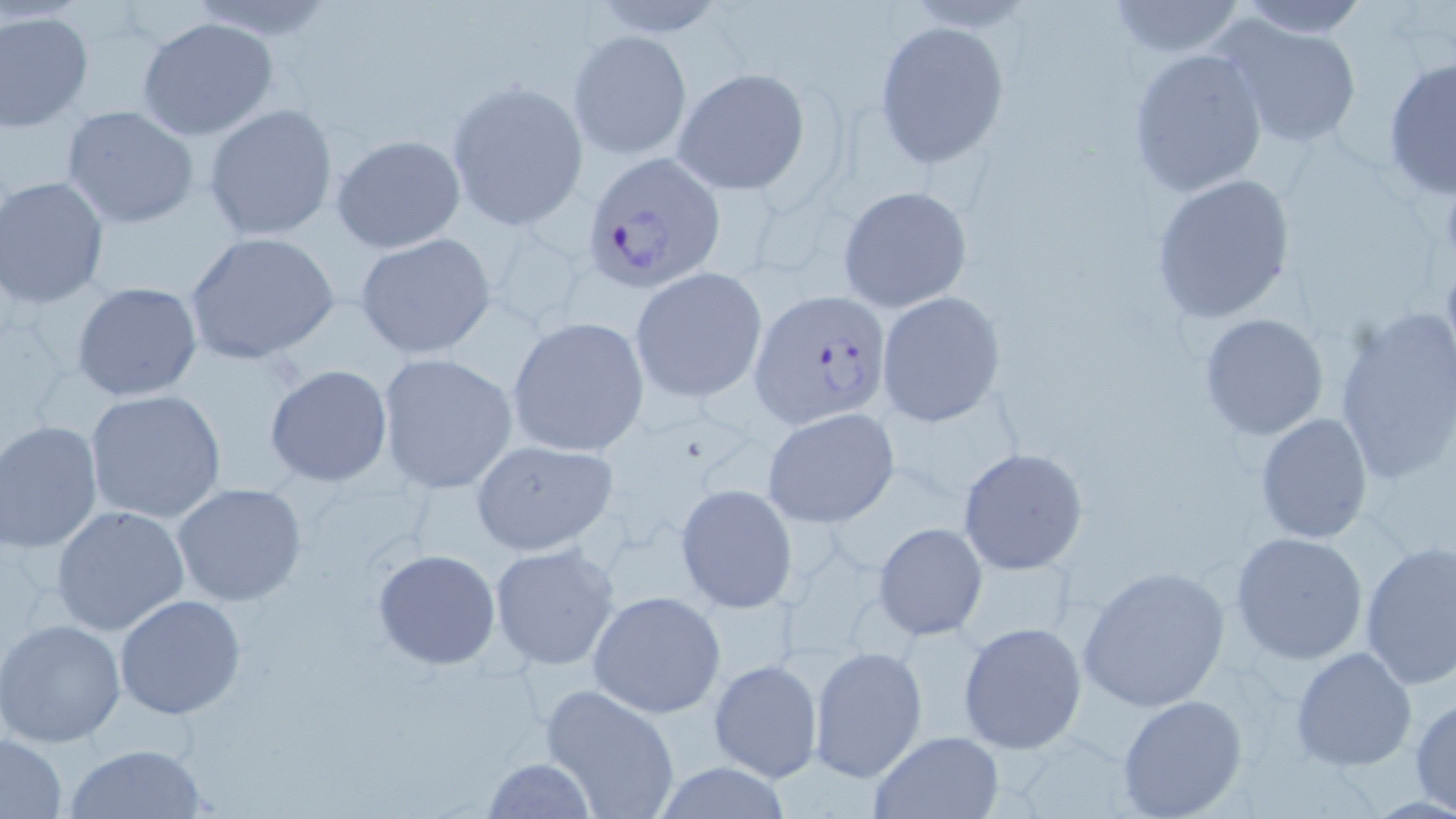
Summary:
  - Coordinate format: approximate bounding boxes as (x1, y1, x2, y2) in pixels
  - Uninfected red blood cell locations: (1102, 0, 1249, 59), (1228, 0, 1371, 37), (0, 10, 94, 131), (1217, 16, 1364, 150), (136, 17, 278, 141), (873, 18, 1009, 168), (568, 30, 692, 162), (1127, 46, 1269, 199), (1382, 57, 1455, 201), (671, 67, 812, 195), (445, 80, 586, 230), (203, 104, 338, 242), (62, 105, 199, 229), (330, 133, 467, 252), (1149, 173, 1296, 325), (1, 175, 110, 308), (837, 185, 973, 313), (184, 232, 340, 365), (354, 234, 497, 360), (629, 267, 767, 403), (71, 281, 203, 403), (874, 292, 1006, 427), (1333, 311, 1454, 488), (1198, 312, 1329, 441), (507, 316, 651, 457), (376, 352, 519, 494), (264, 365, 394, 488), (84, 389, 227, 525), (761, 407, 899, 529), (1256, 410, 1373, 545), (0, 420, 103, 553), (468, 438, 621, 558), (957, 446, 1090, 577), (171, 483, 309, 607), (675, 483, 797, 613), (50, 505, 190, 635), (873, 522, 988, 641), (1229, 530, 1369, 665), (1358, 540, 1456, 689), (488, 542, 623, 671), (372, 548, 501, 670), (1076, 564, 1230, 712), (588, 590, 727, 719), (114, 595, 246, 721), (0, 620, 127, 747), (957, 620, 1087, 754), (808, 645, 927, 782), (1290, 646, 1418, 771), (708, 657, 824, 784), (538, 683, 681, 819), (1116, 694, 1250, 818), (1409, 696, 1456, 814), (868, 730, 1003, 818), (0, 733, 68, 816), (63, 742, 210, 818), (481, 758, 598, 817), (646, 762, 798, 818)
  - Plasmodium falciparum-infected red blood cell locations: (580, 150, 726, 292), (748, 289, 892, 429)
  - Slide-level diagnosis: Plasmodium falciparum
  - Preparation: thin blood film
  - Image size: 1456×819 pixels
  - Magnification: 1000x
  - Modality: light microscopy
  - Field of view: one of a larger specimen
  - Stain: May-Grünwald-Giemsa